Identify the cell.
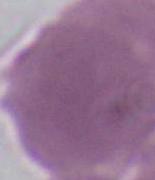

An erythrocyte.

Summary:
  - Modality: photomicrograph
  - Magnification: 1000x